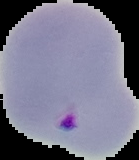

Segmented cell region on a black background. From a thin blood film. Result: malaria parasites identified. Image is 139×160 pixels.